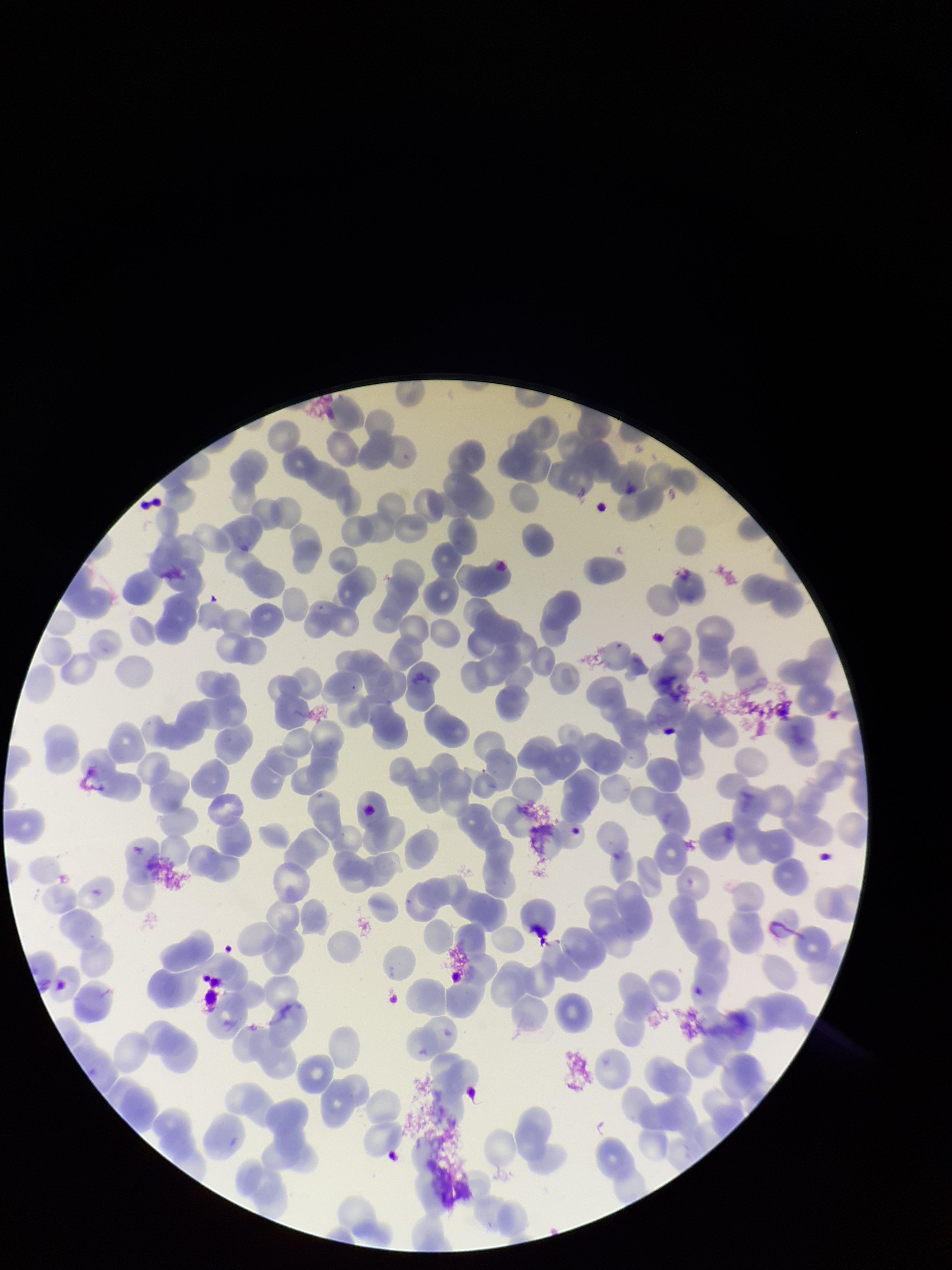
parasitized_red_blood_cells: none identified
parasitized_red_blood_cell_count: 0
field_of_view: one from this slide
stain: Giemsa
patient_malaria_status: positive
red_blood_cell_count: 204
preparation: thin smear
capture: smartphone photograph through the microscope eyepiece
image_size: 952×1270 pixels
species_reported_for_this_patient: Plasmodium falciparum